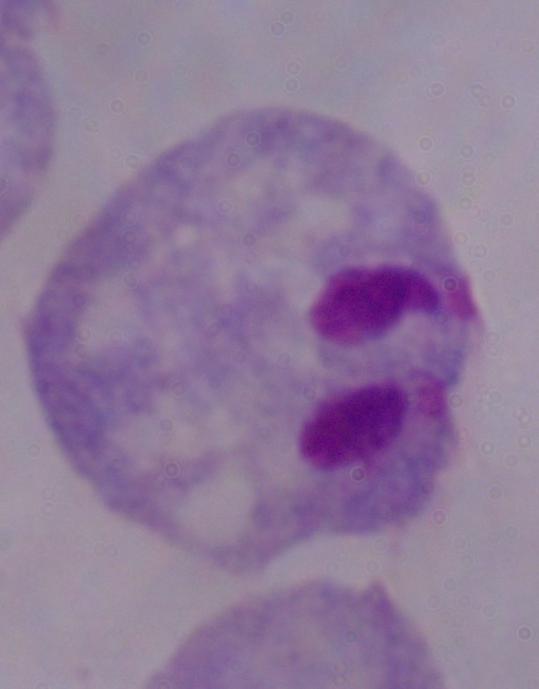 Photomicrograph. 1000x magnification. A trichomonad is seen.